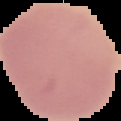

{
  "image_type": "segmented cell region with the area outside set to black",
  "preparation": "thin blood film",
  "image_size": "121×121 pixels",
  "malaria_status": "uninfected"
}